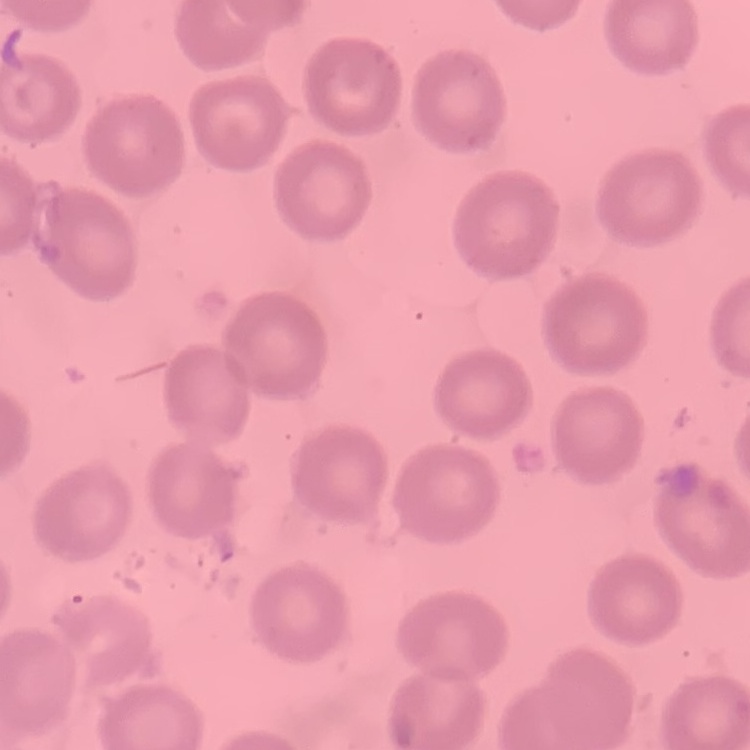

The erythrocytes exhibit no rouleaux formation. Field's or Giemsa stain. Thin blood film. One tile cut from a larger photomicrograph.